Comment on the morphology of the erythrocytes.
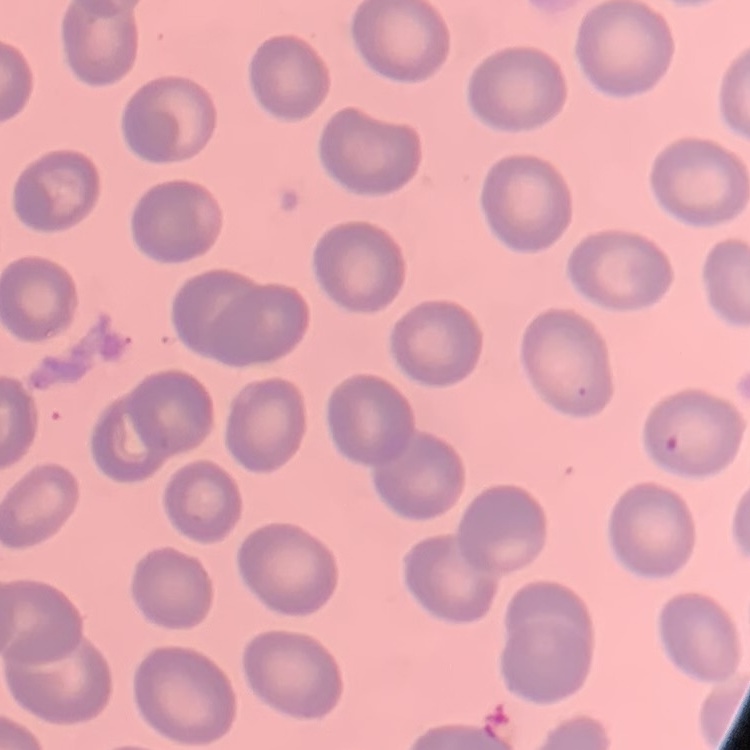

No rouleaux formation.

preparation: thin blood film
stain: Field's or Giemsa
image_type: one tile cut from a larger photomicrograph